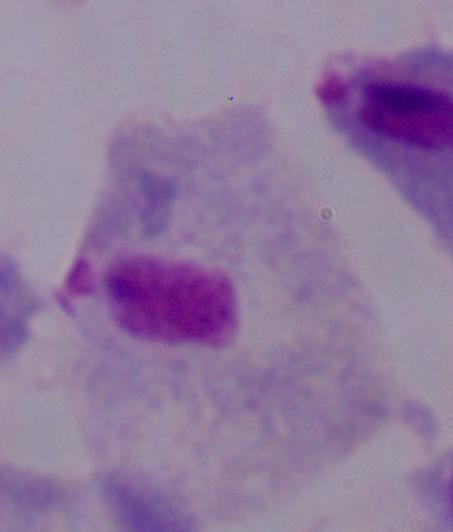
modality: micrograph
magnification: 1000x
identification: trichomonad